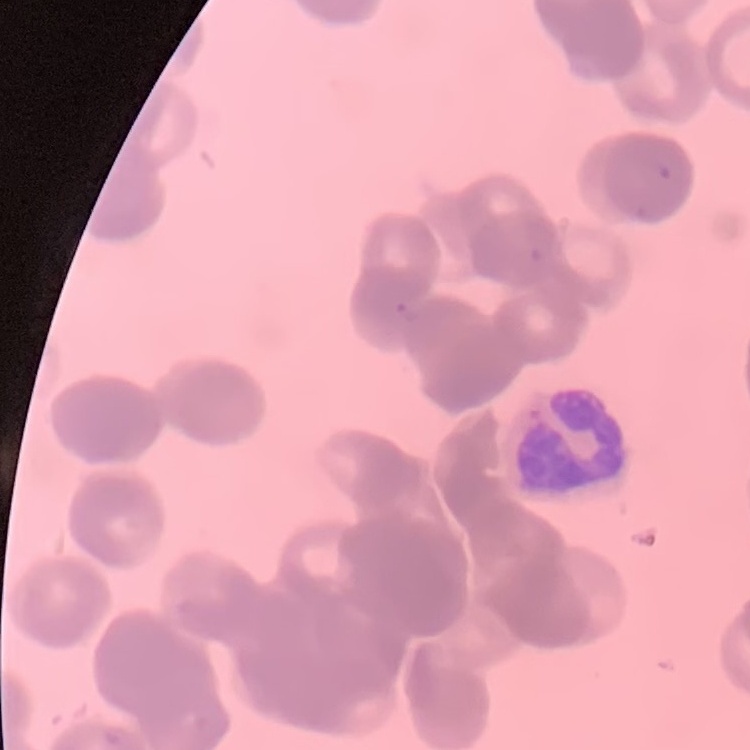 The red blood cells exhibit rouleaux formation. Field's or Giemsa stain. One tile cut from a larger photomicrograph. Thin peripheral smear.